Outline each Plasmodium ovale-infected red blood cell.
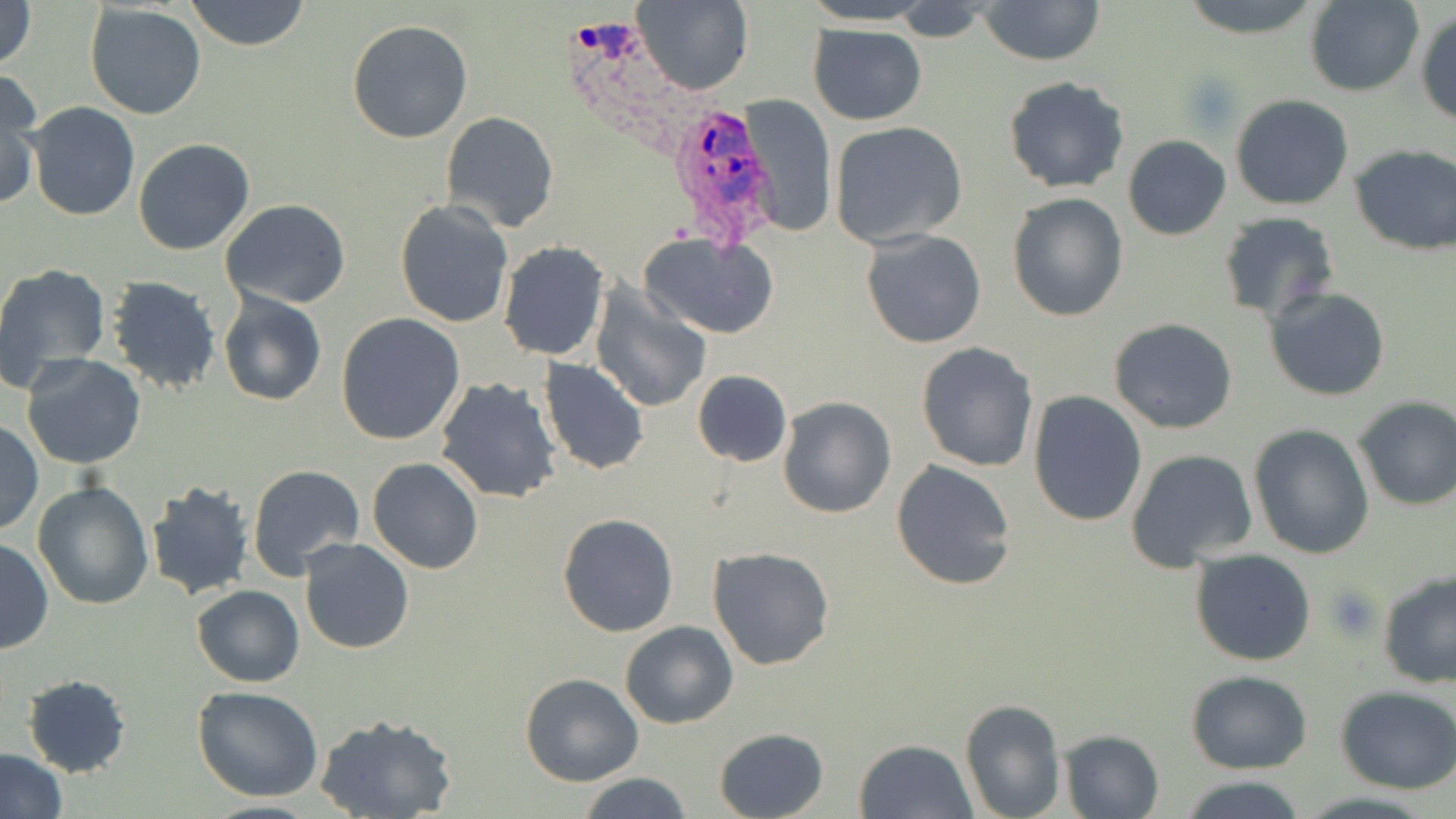
Approximate bounding boxes as (x1,y1)-(x2,y2) corner pairs in pixels.
Plasmodium ovale-infected red blood cells: (568,16)-(690,158), (668,98)-(780,247).

Uninfected red blood cell locations: (186,0)-(310,51), (631,0)-(750,96), (976,0)-(1107,66), (1177,0)-(1325,39), (0,1)-(38,71), (1306,1)-(1424,97), (83,3)-(207,120), (890,4)-(993,44), (1416,8)-(1456,126), (347,18)-(474,144), (809,24)-(927,124), (0,73)-(44,209), (1002,76)-(1130,193), (739,95)-(837,237), (1230,95)-(1353,210), (26,102)-(140,221), (440,111)-(560,233), (829,121)-(968,247), (1122,135)-(1232,240), (133,138)-(254,256), (1349,143)-(1456,256), (1007,192)-(1127,321), (218,199)-(350,309), (394,200)-(513,328), (1217,211)-(1340,321), (862,229)-(985,349), (641,233)-(779,340), (497,241)-(611,362), (0,264)-(112,397), (104,275)-(223,395), (588,284)-(712,414), (1264,286)-(1390,402), (216,292)-(327,407), (335,312)-(466,446), (1108,318)-(1239,435), (916,342)-(1038,471), (21,354)-(147,471), (539,357)-(650,475), (691,370)-(793,468), (433,378)-(562,504), (1028,393)-(1147,525), (1352,395)-(1456,511), (777,396)-(896,518), (1,419)-(43,535), (1248,423)-(1375,558), (1125,448)-(1259,570), (367,457)-(483,574), (891,459)-(1018,591), (246,464)-(365,581), (33,481)-(156,611), (146,482)-(254,600), (557,513)-(679,638), (0,539)-(53,654), (299,539)-(416,655), (708,547)-(835,670), (1190,549)-(1316,666), (1377,569)-(1456,689), (192,585)-(305,687), (619,621)-(739,729), (1187,671)-(1313,773), (22,674)-(132,776), (519,674)-(644,787), (1334,684)-(1456,794), (192,685)-(325,802), (958,698)-(1065,819), (314,714)-(458,819), (713,727)-(830,819), (1057,728)-(1163,818), (853,738)-(979,819), (1,749)-(67,818), (577,772)-(695,819), (1180,775)-(1311,819), (195,800)-(327,819). Platelet locations: (1325,582)-(1381,641). Slide-level diagnosis: Plasmodium ovale. Single field of view. May-Grünwald-Giemsa stain. Thin blood film. Image is 1456×819 pixels. 1000x magnification. Light microscopy.